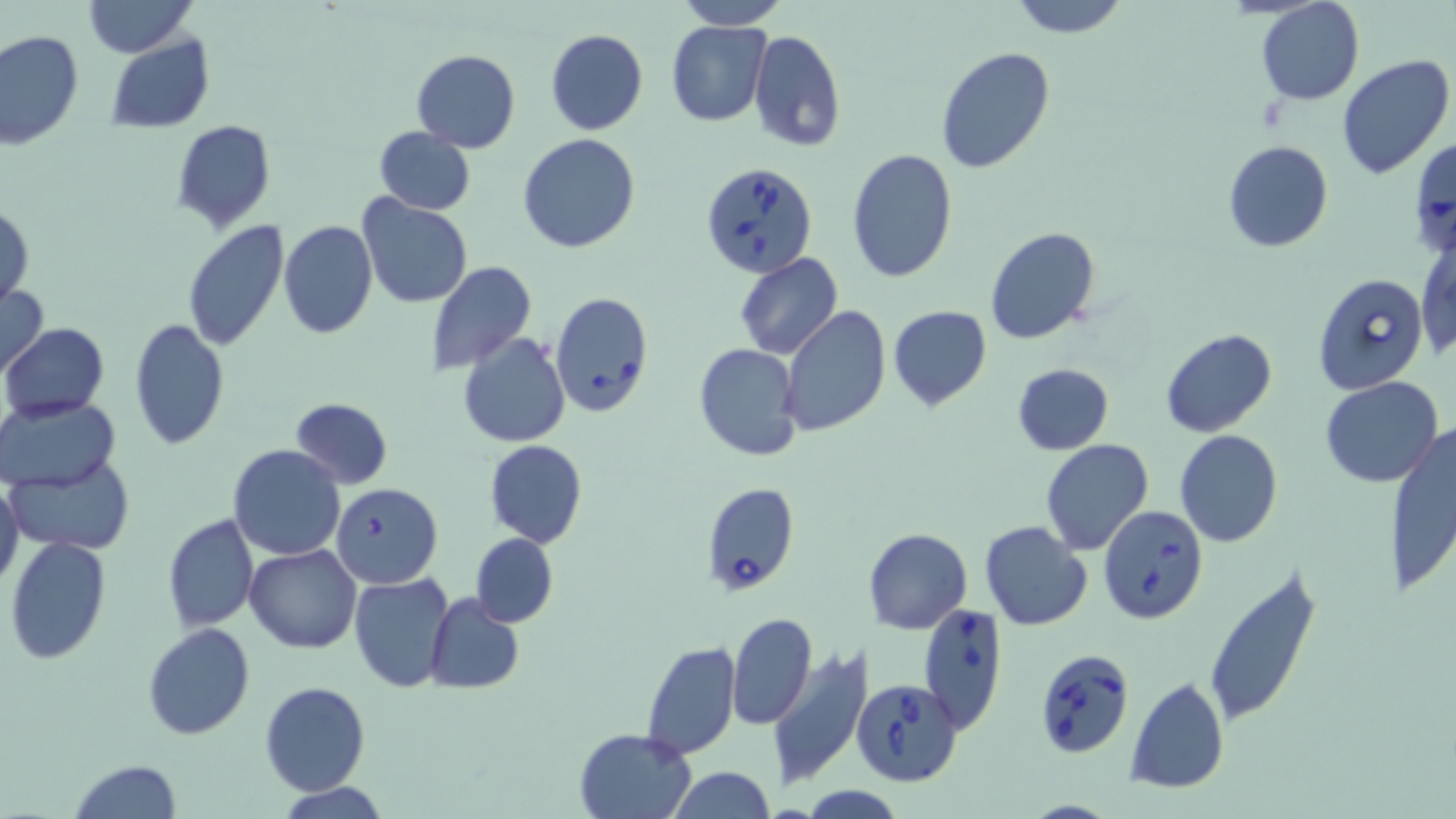
Summary:
  - Coordinate format: approximate bounding boxes as named x1/y1/x2/y2 corners in pixels
  - Babesia divergens-infected red blood cell locations: (x1=700, y1=162, x2=818, y2=280), (x1=1313, y1=272, x2=1431, y2=396), (x1=549, y1=292, x2=654, y2=417), (x1=700, y1=481, x2=799, y2=596), (x1=1097, y1=505, x2=1207, y2=623), (x1=918, y1=603, x2=1008, y2=733), (x1=1042, y1=654, x2=1133, y2=759), (x1=858, y1=680, x2=963, y2=789)
  - Uninfected red blood cell locations: (x1=83, y1=0, x2=196, y2=57), (x1=677, y1=0, x2=787, y2=28), (x1=1006, y1=0, x2=1130, y2=39), (x1=1255, y1=0, x2=1363, y2=105), (x1=665, y1=20, x2=770, y2=126), (x1=545, y1=29, x2=648, y2=135), (x1=747, y1=30, x2=846, y2=152), (x1=0, y1=31, x2=83, y2=151), (x1=104, y1=35, x2=216, y2=132), (x1=935, y1=46, x2=1055, y2=174), (x1=411, y1=48, x2=521, y2=153), (x1=1336, y1=54, x2=1455, y2=178), (x1=171, y1=120, x2=275, y2=231), (x1=372, y1=125, x2=475, y2=217), (x1=517, y1=134, x2=641, y2=254), (x1=1409, y1=135, x2=1456, y2=261), (x1=1224, y1=141, x2=1332, y2=252), (x1=846, y1=148, x2=958, y2=283), (x1=358, y1=196, x2=471, y2=309), (x1=1, y1=201, x2=33, y2=308), (x1=277, y1=219, x2=379, y2=339), (x1=180, y1=221, x2=288, y2=354), (x1=985, y1=227, x2=1101, y2=346), (x1=1417, y1=230, x2=1455, y2=365), (x1=734, y1=253, x2=841, y2=361), (x1=427, y1=261, x2=536, y2=377), (x1=0, y1=283, x2=49, y2=380), (x1=779, y1=306, x2=890, y2=437), (x1=889, y1=306, x2=991, y2=410), (x1=128, y1=319, x2=229, y2=450), (x1=2, y1=323, x2=109, y2=421), (x1=1160, y1=328, x2=1278, y2=439), (x1=459, y1=333, x2=569, y2=447), (x1=694, y1=343, x2=804, y2=461), (x1=1012, y1=363, x2=1113, y2=455), (x1=1320, y1=377, x2=1443, y2=488), (x1=2, y1=396, x2=120, y2=491), (x1=289, y1=397, x2=394, y2=489), (x1=1387, y1=419, x2=1456, y2=600), (x1=1173, y1=430, x2=1283, y2=547), (x1=484, y1=439, x2=588, y2=547), (x1=1040, y1=439, x2=1154, y2=555), (x1=226, y1=445, x2=347, y2=562), (x1=7, y1=454, x2=134, y2=556), (x1=0, y1=478, x2=25, y2=592), (x1=331, y1=483, x2=443, y2=588), (x1=162, y1=513, x2=259, y2=632), (x1=980, y1=520, x2=1094, y2=632), (x1=865, y1=528, x2=972, y2=634), (x1=471, y1=534, x2=558, y2=626), (x1=5, y1=535, x2=113, y2=665), (x1=244, y1=544, x2=361, y2=653), (x1=1204, y1=562, x2=1323, y2=727), (x1=350, y1=572, x2=455, y2=692), (x1=424, y1=594, x2=524, y2=695), (x1=729, y1=613, x2=817, y2=726), (x1=142, y1=622, x2=256, y2=741), (x1=639, y1=639, x2=741, y2=762), (x1=767, y1=646, x2=873, y2=790), (x1=1125, y1=676, x2=1229, y2=795), (x1=259, y1=681, x2=369, y2=797), (x1=575, y1=727, x2=695, y2=818), (x1=67, y1=758, x2=181, y2=819), (x1=668, y1=767, x2=775, y2=819), (x1=279, y1=783, x2=390, y2=819)
  - Slide-level diagnosis: Babesia divergens
  - Field of view: one of a larger specimen
  - Image size: 1456×819 pixels
  - Stain: May-Grünwald-Giemsa
  - Preparation: thin blood film
  - Magnification: 1000x
  - Modality: light microscopy